State which cell type is depicted.
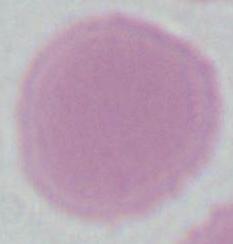

This is an erythrocyte.

magnification = 1000x
modality = photomicrograph